Identify the parasite.
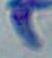

Toxoplasma gondii.

Summary:
  - Modality: photomicrograph
  - Magnification: 1000x